State which parasite is depicted.
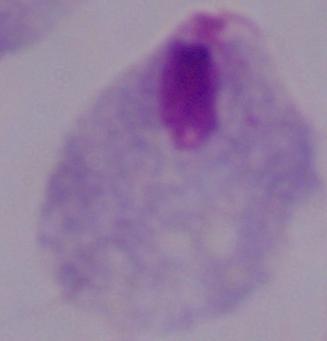

This is a trichomonad.

magnification = 1000x
modality = photomicrograph